Classify this cell by malaria status.
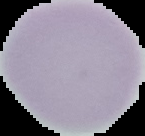
It is uninfected.

Summary:
  - Image size: 145×136 pixels
  - Image type: segmented cell region on a black background
  - Preparation: thin blood smear